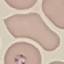

Summary:
  - Malaria status: parasitized
  - Image type: cell patch, automatically extracted from a larger field of view and resized to 64 × 64 pixels
  - Stain: Giemsa
  - Preparation: thin smear
  - Capture: smartphone through the microscope eyepiece